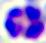

magnification = 400x
modality = micrograph
identification = leukocyte